Assess this cell for malaria.
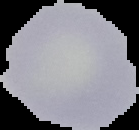

It is uninfected.

Summary:
  - Image size: 139×130 pixels
  - Image type: segmented cell region on a black background
  - Preparation: thin blood film